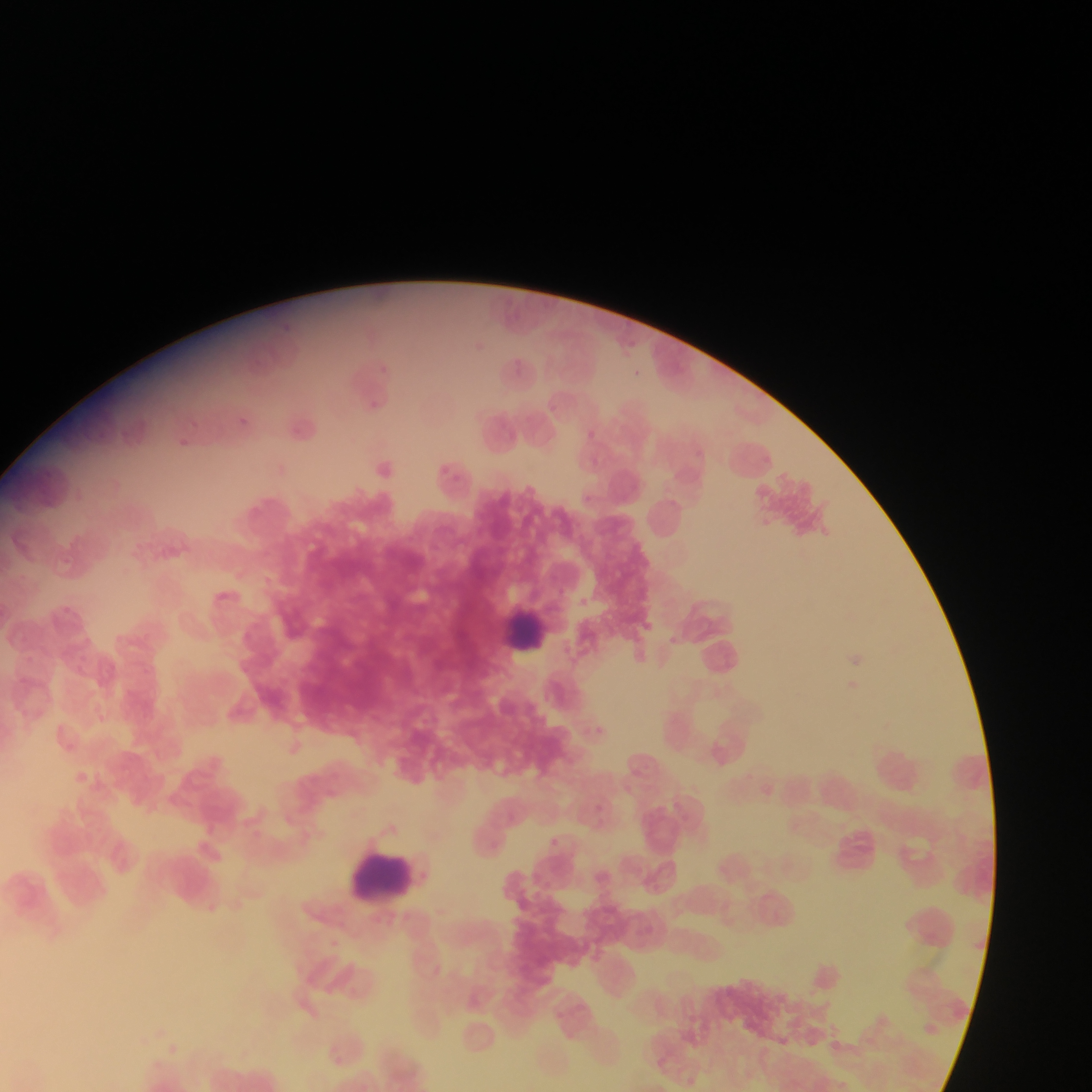

Approximate bounding boxes as {left, top, right, bottom} in pixels. Leukocyte locations: {500, 602, 558, 668}, {867, 742, 933, 803}, {344, 845, 425, 911}. Plasmodium parasite locations: {279, 316, 293, 334}, {513, 357, 525, 377}, {370, 400, 384, 414}, {549, 403, 565, 421}, {237, 411, 251, 429}, {589, 429, 600, 441}, {178, 434, 196, 454}, {582, 492, 608, 506}, {670, 629, 687, 651}, {850, 653, 873, 673}, {595, 722, 609, 738}, {545, 836, 560, 852}. Mobile-phone photograph taken through the microscope. Image is 1092×1092 pixels. Single field of view. Collected in Ghana. Thin blood film.